Name the parasite shown.
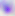
Toxoplasma gondii.

Captured at 400x magnification. Photomicrograph.